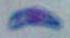

Summary:
  - Identification: Toxoplasma gondii
  - Magnification: 1000x
  - Modality: photomicrograph